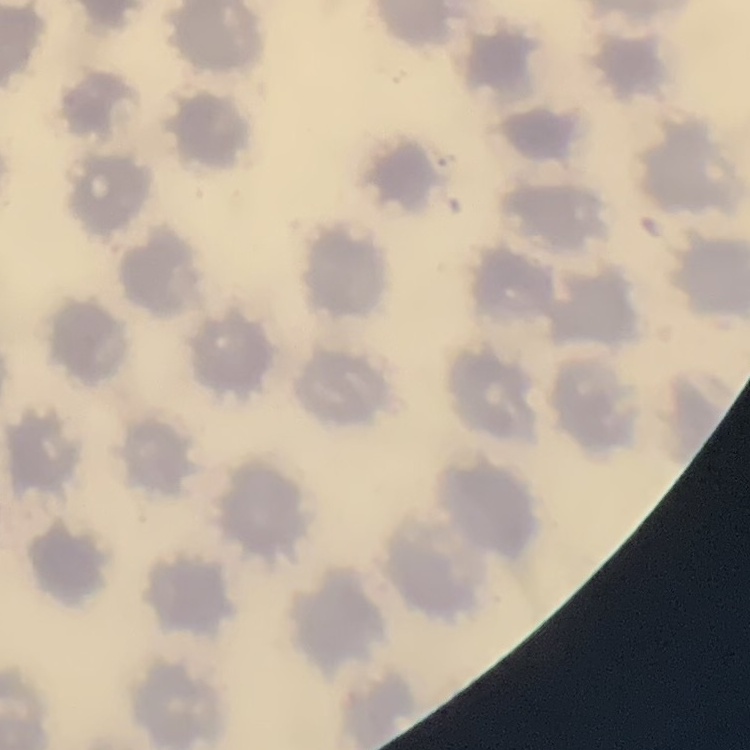
Summary:
  - Erythrocyte morphology: no rouleaux formation
  - Image type: one tile cut from a larger photomicrograph
  - Stain: Field's or Giemsa
  - Preparation: thin blood film